Report the malaria status of this cell.
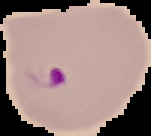

It is parasitized.

Cell region segmented out of the field of view; the surrounding area is masked to black. Image is 151×136 pixels. From a thin blood film.